Locate and identify every blood parasite.
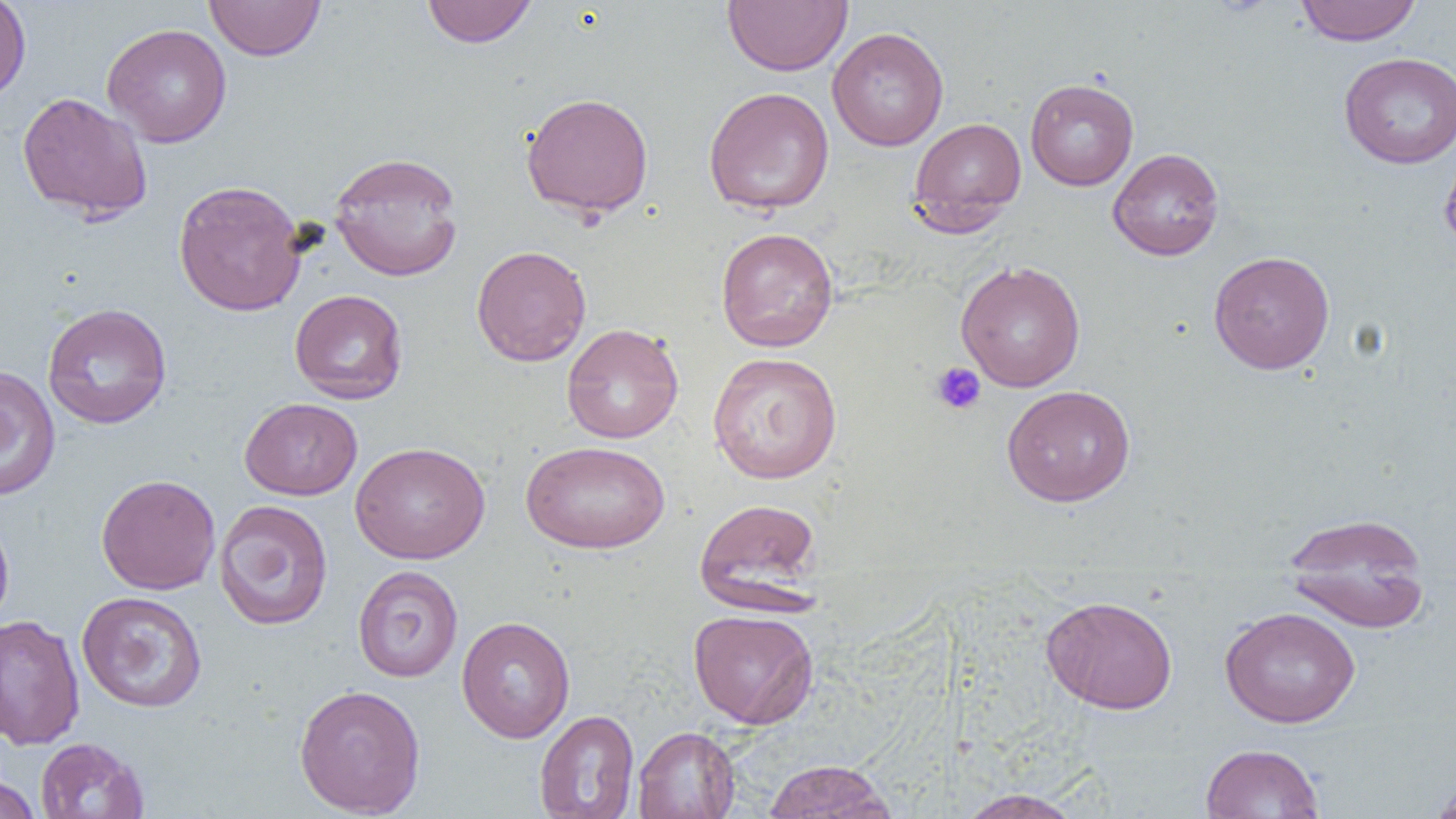
No blood parasites observed.

Approximate bounding boxes as (x1,y1)-(x2,y2) corner pairs in pixels. Platelet locations: (930,362)-(987,416). Uninfected red blood cell locations: (0,0)-(31,105), (205,0)-(326,61), (723,0)-(852,76), (1294,0)-(1422,46), (420,1)-(538,48), (102,23)-(232,148), (827,27)-(948,151), (1339,51)-(1456,169), (1025,78)-(1139,191), (703,87)-(834,214), (17,91)-(153,223), (520,92)-(655,218), (908,117)-(1026,232), (1439,139)-(1456,258), (1108,147)-(1224,261), (328,151)-(464,282), (173,179)-(308,317), (715,227)-(839,353), (471,245)-(591,366), (1208,250)-(1335,374), (955,260)-(1086,392), (289,289)-(409,404), (42,302)-(172,430), (561,323)-(684,444), (707,352)-(843,485), (0,365)-(61,501), (1001,384)-(1136,507), (239,397)-(363,500), (521,440)-(670,554), (350,441)-(490,563), (95,474)-(221,595), (694,497)-(823,611), (214,499)-(333,631), (0,508)-(15,634), (1282,511)-(1431,633), (352,565)-(464,682), (76,591)-(208,713), (1040,595)-(1178,714), (1220,606)-(1360,727), (688,609)-(819,728), (0,613)-(85,750), (457,616)-(575,743), (293,684)-(426,817), (534,709)-(639,819), (632,726)-(740,819), (35,737)-(148,819), (1200,743)-(1325,819), (763,759)-(897,819), (0,772)-(41,819), (1428,775)-(1456,819), (957,789)-(1083,818). Slide-level diagnosis: no evidence of blood parasites. One field of a larger specimen. Thin blood smear. Captured at 1000x magnification. Image is 1456×819 pixels. Light microscopy.